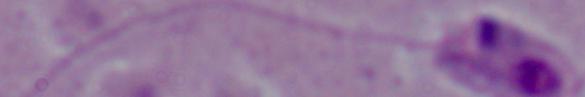

{
  "identification": "Leishmania",
  "magnification": "1000x",
  "modality": "micrograph"
}